Describe the morphology of the red blood cells.
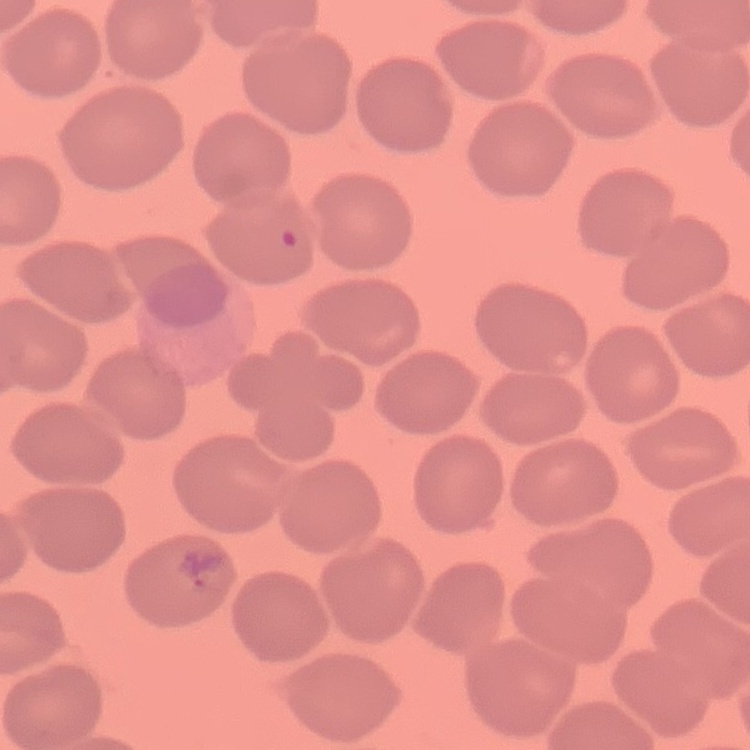

They show no rouleaux formation.

Summary:
  - Image type: one tile cut from a larger photomicrograph
  - Preparation: thin blood film
  - Stain: Field's or Giemsa